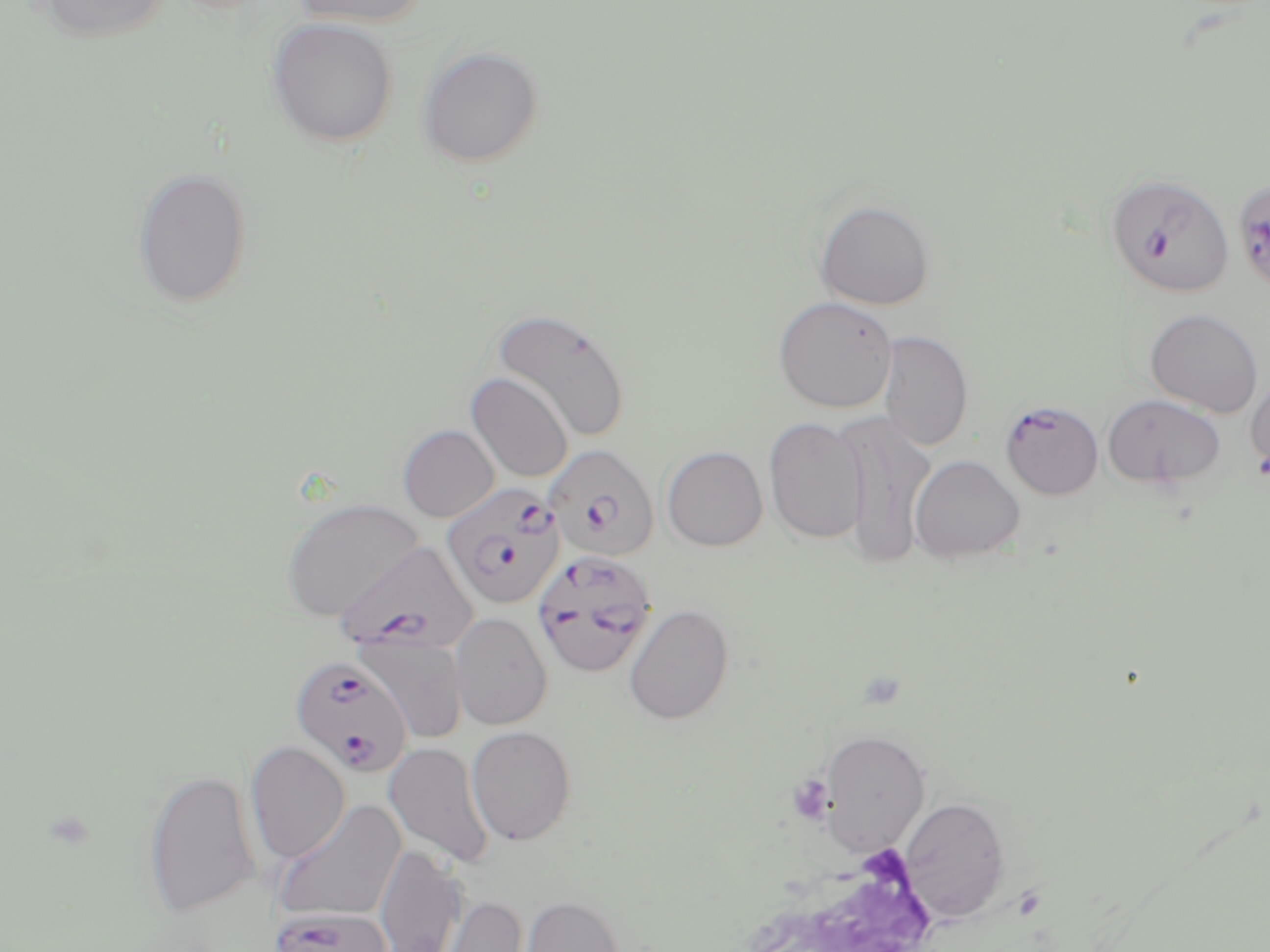

Summary:
  - Coordinate format: approximate bounding boxes as (x1, y1, x2, y2) in pixels
  - Platelet locations: (787, 775, 835, 825)
  - Uninfected red blood cell locations: (33, 0, 174, 43), (287, 0, 430, 28), (267, 17, 398, 147), (418, 45, 544, 167), (132, 167, 252, 308), (814, 200, 935, 310), (772, 295, 898, 413), (491, 307, 632, 444), (1144, 308, 1264, 417), (879, 330, 973, 452), (466, 372, 573, 484), (1244, 374, 1270, 482), (1102, 393, 1226, 489), (833, 411, 936, 571), (763, 416, 868, 544), (398, 424, 500, 522), (661, 445, 768, 551), (908, 454, 1025, 564), (281, 498, 423, 621), (623, 604, 734, 725), (450, 612, 553, 731), (356, 633, 468, 744), (465, 725, 577, 846), (819, 728, 931, 855), (245, 741, 351, 864), (384, 741, 494, 867), (144, 768, 260, 918), (899, 796, 1012, 922), (274, 799, 407, 922), (374, 844, 469, 952), (434, 894, 529, 952), (519, 894, 626, 952)
  - Plasmodium falciparum-infected red blood cell locations: (1105, 171, 1235, 299), (1241, 186, 1270, 293), (999, 400, 1104, 500), (546, 444, 659, 561), (442, 482, 565, 610), (336, 540, 478, 655), (532, 549, 658, 680), (290, 655, 413, 777), (270, 907, 393, 952)
  - Slide-level diagnosis: Plasmodium falciparum
  - Stain: May-Grünwald-Giemsa
  - Preparation: thin blood smear
  - Image size: 1270×952 pixels
  - Field of view: one of a larger specimen
  - Modality: light microscopy
  - Magnification: 1000x